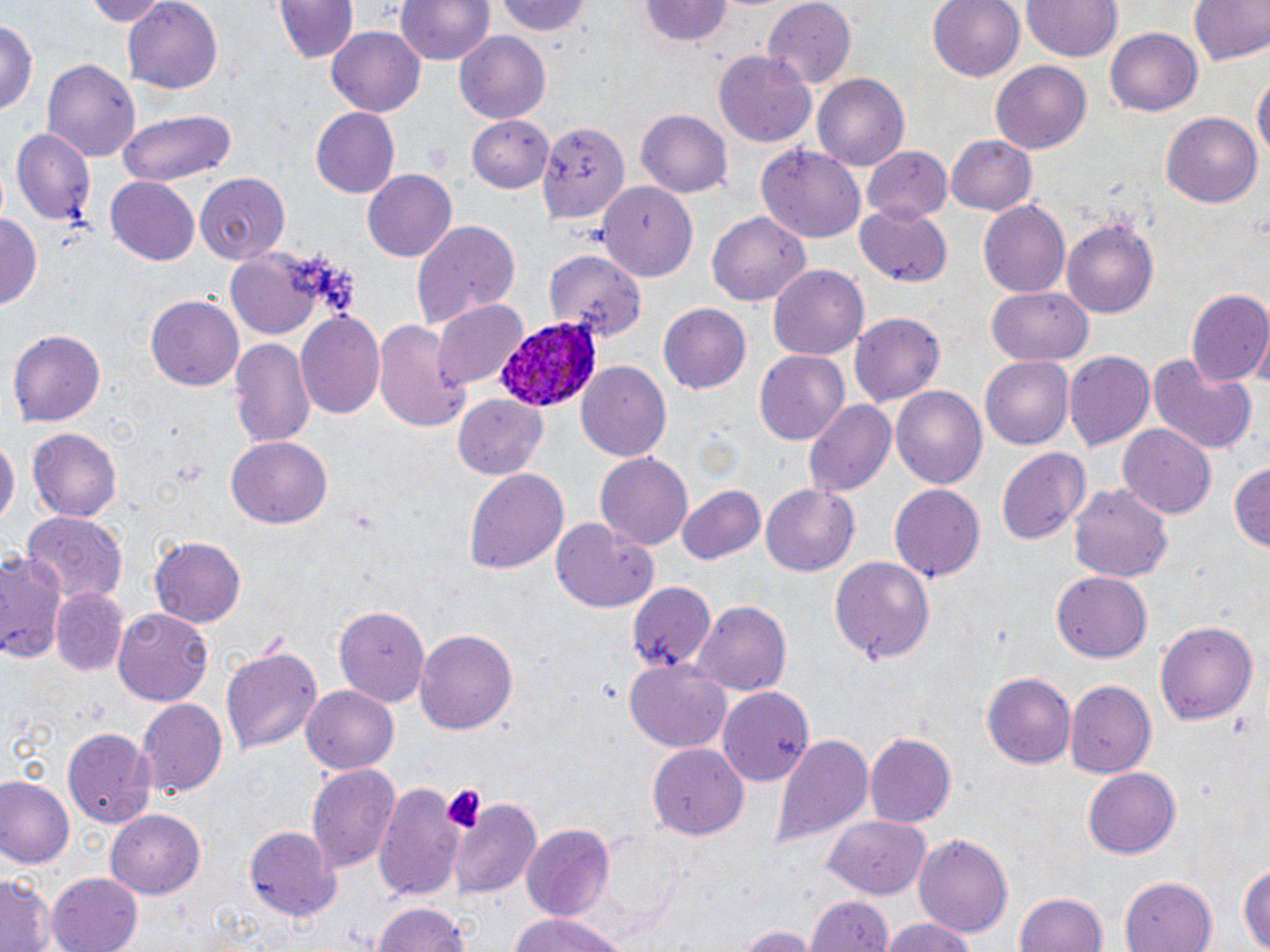

Summary:
  - Coordinate format: approximate bounding boxes as (x1,y1)-(x2,y2) corner pairs in pixels
  - Platelet locations: (441,783)-(487,836)
  - Uninfected red blood cell locations: (83,0)-(168,25), (119,0)-(224,91), (269,0)-(359,67), (392,0)-(497,68), (493,0)-(594,39), (759,0)-(858,88), (927,0)-(1025,82), (1020,0)-(1123,60), (1182,0)-(1270,68), (640,2)-(735,48), (0,17)-(38,121), (327,26)-(426,116), (1104,28)-(1203,116), (454,32)-(551,125), (715,50)-(818,146), (41,58)-(142,162), (991,61)-(1091,156), (1252,67)-(1268,177), (814,74)-(909,173), (310,107)-(400,199), (115,108)-(239,187), (636,110)-(733,196), (1161,112)-(1262,208), (468,115)-(557,191), (540,125)-(630,225), (8,127)-(96,226), (947,133)-(1037,214), (757,145)-(866,243), (865,146)-(952,223), (361,168)-(456,263), (195,171)-(289,267), (104,178)-(201,265), (597,182)-(697,282), (978,200)-(1069,298), (856,201)-(953,284), (707,210)-(812,307), (1,212)-(42,312), (1061,215)-(1159,318), (412,219)-(520,326), (225,248)-(338,338), (548,251)-(647,343), (769,264)-(869,360), (1184,286)-(1270,390), (987,288)-(1092,365), (146,293)-(243,391), (435,300)-(529,390), (659,303)-(752,393), (295,311)-(386,419), (851,313)-(945,408), (373,315)-(472,432), (8,328)-(106,427), (230,336)-(317,451), (754,350)-(849,444), (1062,350)-(1156,452), (1146,353)-(1257,456), (979,357)-(1071,451), (577,361)-(672,463), (891,387)-(986,492), (454,394)-(547,479), (805,399)-(897,497), (1118,423)-(1217,519), (26,428)-(122,521), (0,433)-(17,536), (227,438)-(331,528), (995,446)-(1091,546), (595,450)-(693,550), (1228,462)-(1270,554), (463,468)-(569,574), (1066,479)-(1174,584), (889,482)-(987,582), (761,483)-(859,576), (677,484)-(766,566), (22,509)-(125,604), (549,516)-(660,615), (150,535)-(245,629), (0,551)-(66,663), (830,555)-(936,665), (1053,569)-(1151,660), (624,581)-(741,674), (50,587)-(130,677), (694,601)-(790,697), (335,602)-(435,706), (111,606)-(214,706), (1155,618)-(1260,726), (416,626)-(517,732), (221,642)-(322,757), (624,659)-(731,753), (983,671)-(1076,770), (1064,679)-(1157,778), (300,685)-(400,775), (718,685)-(817,785), (137,696)-(226,795), (62,723)-(155,827), (866,732)-(956,826), (771,734)-(875,848), (648,742)-(748,839), (308,763)-(402,875), (1082,766)-(1182,859), (0,778)-(74,867), (373,782)-(467,900), (451,796)-(539,896), (103,807)-(205,898), (825,815)-(934,899), (245,823)-(341,918), (519,824)-(614,922), (914,832)-(1012,941), (1239,858)-(1269,950), (45,871)-(143,952), (1119,873)-(1215,952), (0,876)-(54,952), (1014,890)-(1108,951), (801,893)-(896,952), (368,901)-(474,952), (504,914)-(630,952), (878,918)-(985,952), (732,924)-(817,952)
  - Plasmodium ovale-infected red blood cell locations: (497,317)-(603,411)
  - Slide-level diagnosis: Plasmodium ovale
  - Field of view: one of a larger specimen
  - Preparation: thin blood film
  - Magnification: 1000x
  - Stain: May-Grünwald-Giemsa
  - Image size: 1270×952 pixels
  - Modality: light microscopy